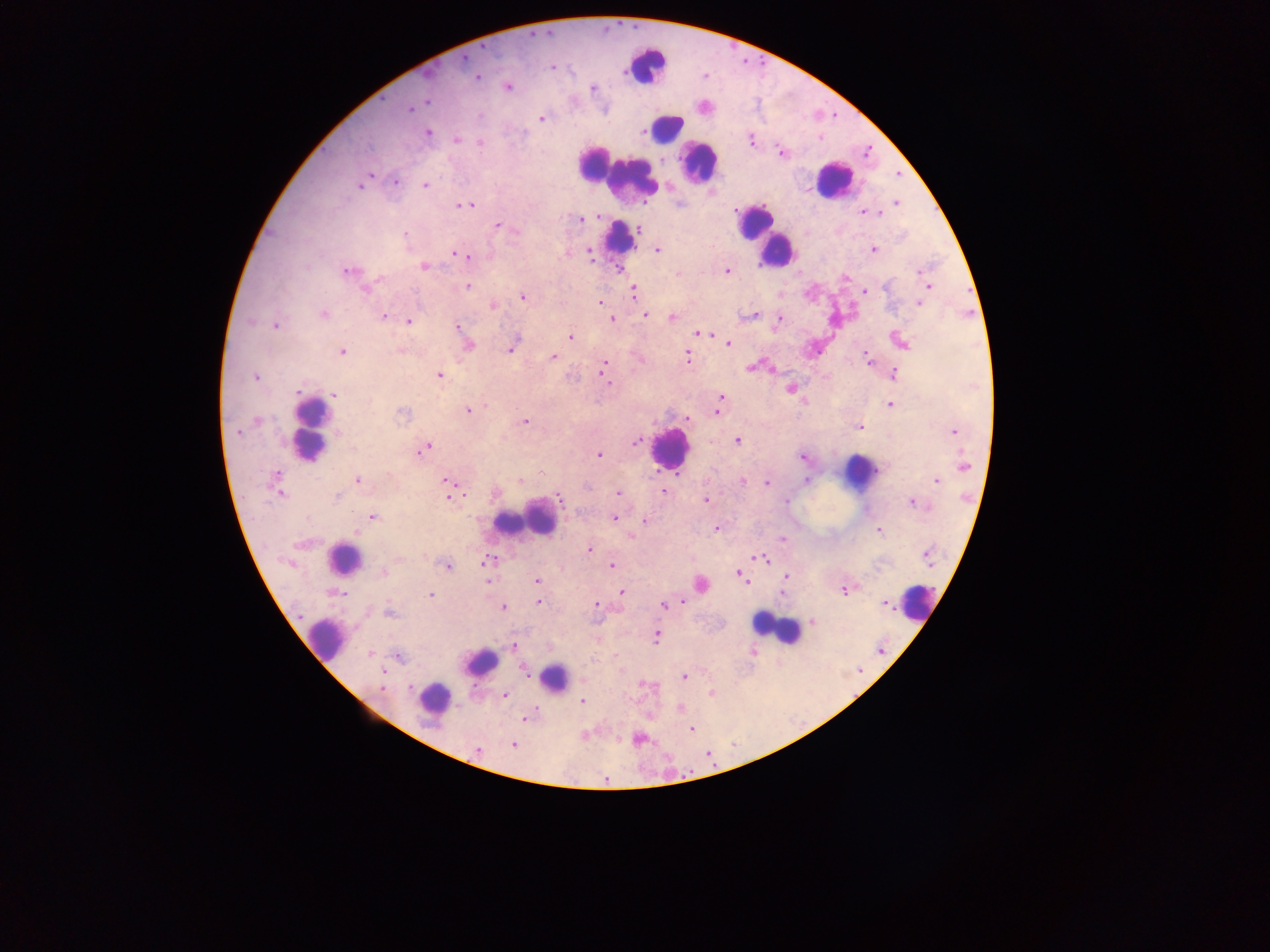
Approximate centers as (x, y) in pixels.
Summary:
  - Leukocyte locations: (646, 65), (666, 128), (593, 162), (699, 162), (604, 169), (630, 179), (832, 179), (619, 236), (766, 236), (312, 432), (669, 448), (858, 472), (537, 519), (516, 522), (343, 559), (918, 602), (775, 627), (325, 637), (482, 662), (554, 678), (432, 698)
  - Plasmodium parasite locations: (465, 58), (552, 68), (478, 77), (507, 88), (593, 88), (427, 101), (410, 109), (542, 119), (428, 133), (456, 140), (750, 141), (480, 143), (781, 152), (371, 174), (395, 182), (424, 185), (361, 186), (896, 202), (471, 204), (460, 205), (864, 213), (875, 213), (600, 217), (580, 219), (498, 225), (638, 229), (515, 231), (405, 234), (656, 250), (874, 250), (455, 253), (590, 253), (464, 256), (424, 266), (348, 270), (727, 271), (919, 272), (846, 277), (379, 278), (467, 286), (926, 287), (367, 290), (864, 291), (634, 292), (522, 297), (600, 303), (920, 303), (493, 306), (323, 315), (754, 315), (383, 316), (646, 316), (672, 317), (612, 318), (780, 319), (409, 322), (275, 325), (457, 326), (699, 332), (571, 337), (727, 343), (901, 343), (469, 346), (510, 349), (342, 352), (401, 352), (687, 356), (553, 357), (867, 359), (603, 367), (750, 367), (894, 374), (439, 375), (255, 377), (607, 380), (790, 389), (298, 391), (335, 394), (721, 397), (719, 404), (891, 405), (468, 411), (716, 412), (403, 414), (687, 418), (257, 420), (525, 421), (858, 426), (237, 432), (955, 432), (737, 442), (635, 443), (424, 448), (599, 455), (802, 458), (964, 466), (389, 475), (276, 476), (358, 481), (446, 481), (521, 481), (806, 481), (936, 481), (743, 482), (766, 483), (664, 491), (619, 493), (280, 494), (337, 497), (448, 498), (560, 499), (706, 500), (787, 500), (913, 503), (372, 517), (614, 518), (645, 521), (716, 529), (879, 530), (356, 531), (783, 539), (589, 549), (758, 557), (927, 557), (764, 559), (489, 561), (611, 565), (447, 566), (383, 572), (739, 573), (786, 577), (537, 580), (702, 585), (844, 589), (622, 592), (337, 593), (782, 593), (431, 595), (539, 603), (885, 603), (596, 604), (663, 606), (503, 607), (389, 612), (813, 621), (656, 637), (513, 646), (370, 654), (398, 657), (524, 671), (684, 676), (382, 677), (410, 686), (382, 688), (712, 693), (505, 695), (582, 701), (680, 708), (524, 720), (691, 728), (638, 739), (514, 745), (477, 749)
  - Image size: 1270×952 pixels
  - Field of view: single
  - Preparation: thick blood smear
  - Capture: mobile-phone photograph through a microscope
  - Country: Ghana